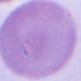
Micrograph. An erythrocyte is shown. 1000x magnification.